Point out each Plasmodium parasite.
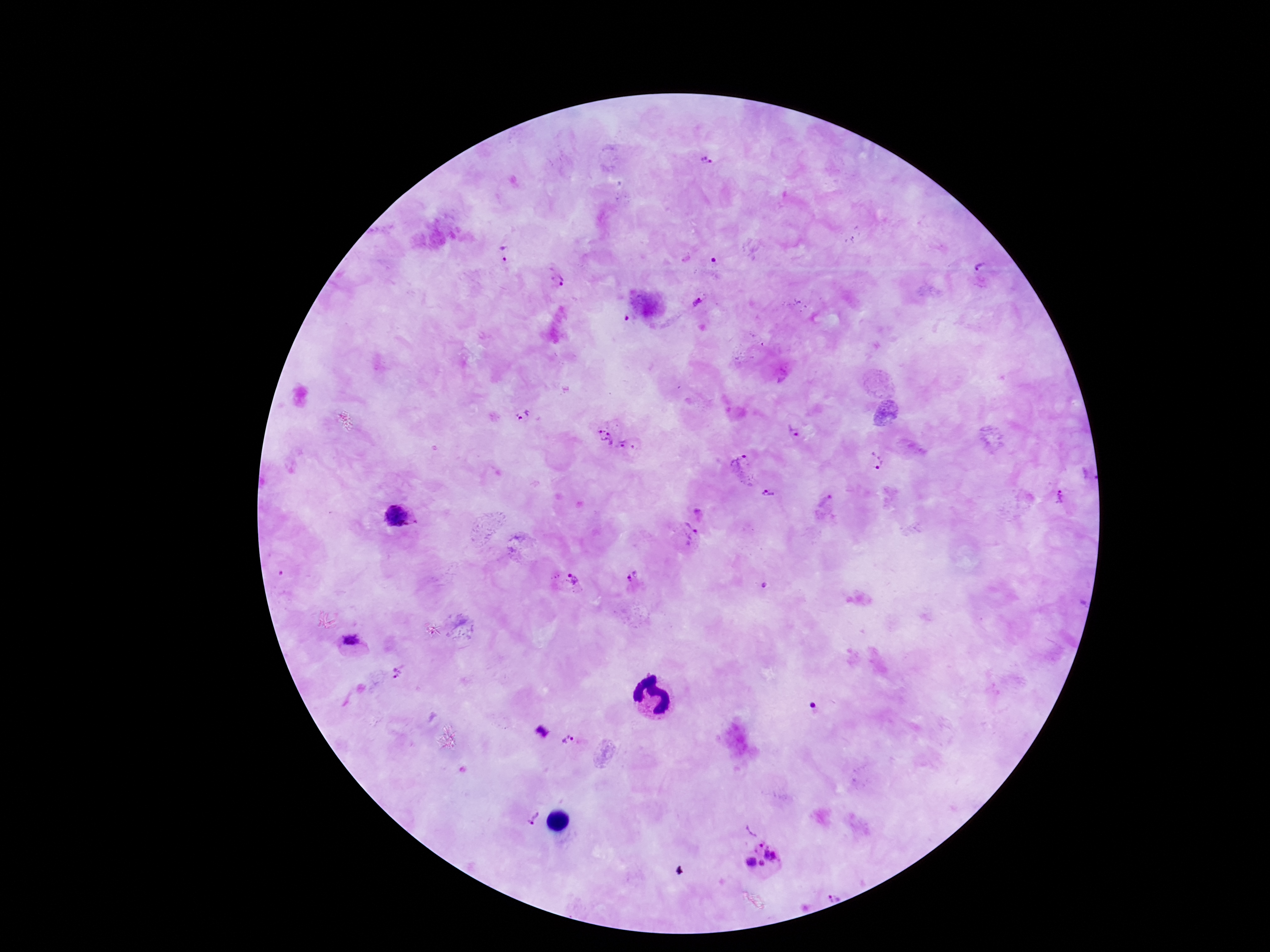

Approximate object centers, in pixels from the top-left corner.
Plasmodium parasites: (x=704, y=162), (x=504, y=256), (x=981, y=269), (x=558, y=280), (x=702, y=301), (x=525, y=417), (x=793, y=433), (x=602, y=435), (x=632, y=450), (x=874, y=461), (x=741, y=471), (x=771, y=494), (x=1062, y=498), (x=827, y=502), (x=702, y=514), (x=400, y=518), (x=686, y=537), (x=633, y=579), (x=571, y=580), (x=764, y=587), (x=352, y=641), (x=400, y=670), (x=538, y=729), (x=573, y=740), (x=528, y=814), (x=763, y=859), (x=835, y=890).

Giemsa stain. Patient malaria status: infected. Thick blood smear. 100x magnification. Photographed through the microscope eyepiece with a smartphone camera. One field from this slide. Image is 1270×952 pixels.